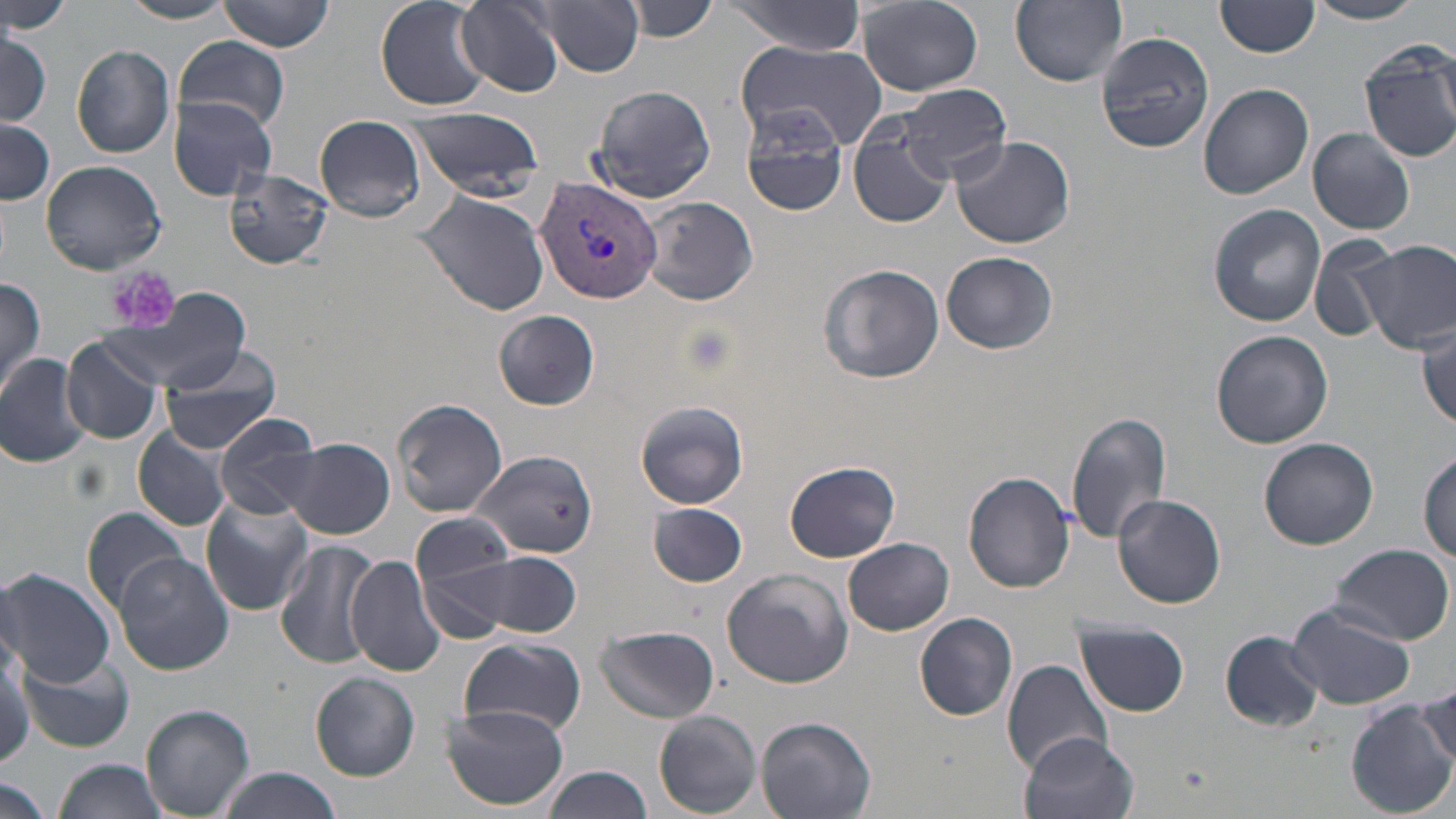 Approximate bounding boxes as (x1, y1, x2, y2) in pixels. Uninfected red blood cell locations: (1, 0, 74, 37), (119, 0, 241, 23), (217, 0, 334, 53), (376, 0, 490, 112), (533, 0, 645, 76), (629, 0, 721, 41), (727, 0, 867, 55), (1011, 0, 1128, 87), (856, 1, 983, 95), (1308, 1, 1426, 24), (453, 2, 564, 99), (1214, 2, 1319, 59), (0, 29, 50, 127), (1095, 30, 1214, 155), (170, 37, 290, 129), (730, 41, 886, 154), (1358, 41, 1456, 163), (72, 46, 175, 158), (1199, 82, 1314, 199), (895, 83, 1013, 182), (589, 84, 717, 205), (167, 95, 280, 199), (407, 109, 545, 193), (741, 109, 847, 216), (314, 115, 426, 222), (0, 119, 54, 205), (847, 122, 953, 229), (1308, 127, 1416, 235), (949, 134, 1076, 248), (40, 159, 167, 274), (224, 170, 333, 270), (417, 191, 552, 316), (636, 195, 759, 306), (1207, 203, 1326, 326), (1309, 235, 1405, 340), (1358, 240, 1456, 355), (941, 252, 1059, 354), (818, 263, 945, 384), (0, 275, 47, 399), (100, 292, 255, 390), (494, 310, 598, 410), (1416, 325, 1455, 432), (1210, 329, 1334, 448), (62, 336, 163, 446), (156, 342, 285, 456), (0, 352, 93, 468), (393, 398, 510, 518), (635, 400, 749, 511), (1065, 411, 1172, 544), (213, 412, 322, 519), (134, 426, 232, 532), (1257, 437, 1378, 549), (285, 439, 394, 538), (1419, 446, 1456, 563), (475, 449, 601, 559), (784, 460, 900, 562), (964, 470, 1076, 593), (1112, 495, 1226, 608), (200, 496, 314, 615), (646, 501, 749, 587), (82, 507, 192, 614), (412, 513, 518, 595), (843, 538, 955, 636), (275, 539, 378, 668), (1328, 543, 1454, 644), (458, 550, 584, 638), (345, 553, 445, 678), (114, 554, 234, 675), (0, 566, 116, 686), (720, 568, 852, 687), (1288, 601, 1416, 712), (915, 612, 1019, 720), (1075, 620, 1190, 717), (595, 624, 720, 723), (1221, 629, 1325, 732), (0, 634, 33, 770), (458, 638, 586, 736), (20, 648, 135, 753), (1001, 658, 1115, 775), (310, 672, 420, 781), (1416, 681, 1454, 774), (1391, 685, 1456, 796), (1348, 700, 1455, 817), (140, 703, 255, 819), (443, 705, 569, 810), (653, 710, 762, 816), (754, 716, 876, 819), (1021, 731, 1139, 819), (53, 758, 173, 819), (543, 765, 652, 819), (218, 769, 346, 819), (0, 776, 53, 819). Platelet locations: (110, 266, 181, 334). Plasmodium vivax-infected red blood cell locations: (534, 178, 662, 301). Slide-level diagnosis: Plasmodium vivax. Image is 1456×819 pixels. Optical microscopy. Thin blood film. May-Grünwald-Giemsa stain. Single field of view. 1000x magnification.